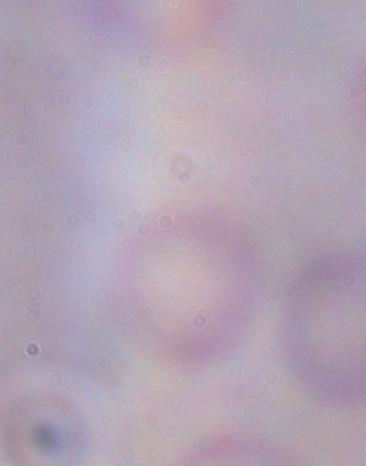

Micrograph. 1000x magnification. A trypanosome is seen.